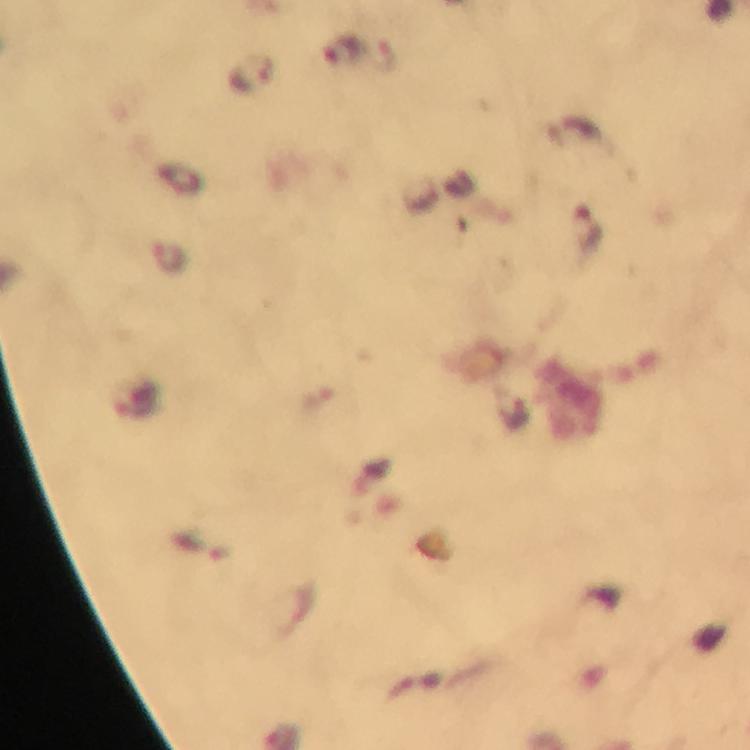

Approximate centers as (x, y) in pixels.
Summary:
  - Plasmodium parasite locations: (344, 51), (251, 76), (588, 229), (202, 549)
  - Magnification: 100x
  - Immersion oil: used
  - Context: from a malaria diagnostic workup
  - Cropped from: a single field of view
  - Stain: Giemsa
  - Capture: smartphone photograph through a microscope
  - Preparation: thick blood smear
  - Image size: 750×750 pixels